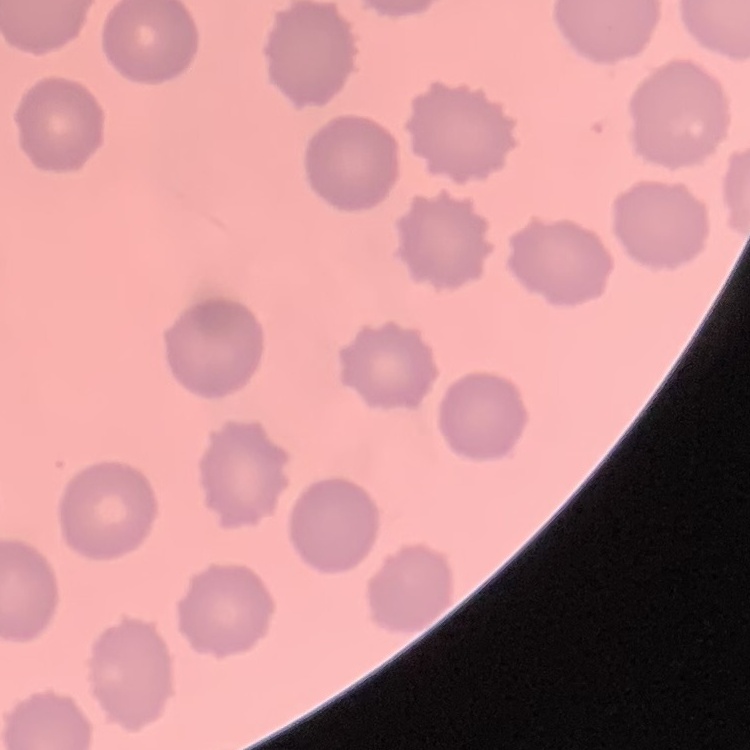
{
  "erythrocyte_morphology": "no rouleaux formation",
  "stain": "Field's or Giemsa",
  "image_type": "square crop of a larger photomicrograph",
  "preparation": "thin peripheral smear"
}